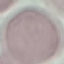 Malaria status: uninfected. Thin smear of blood. Automatically extracted cell patch, resized to 64 × 64 pixels. Acquired by smartphone through the microscope eyepiece. Giemsa-stained preparation.